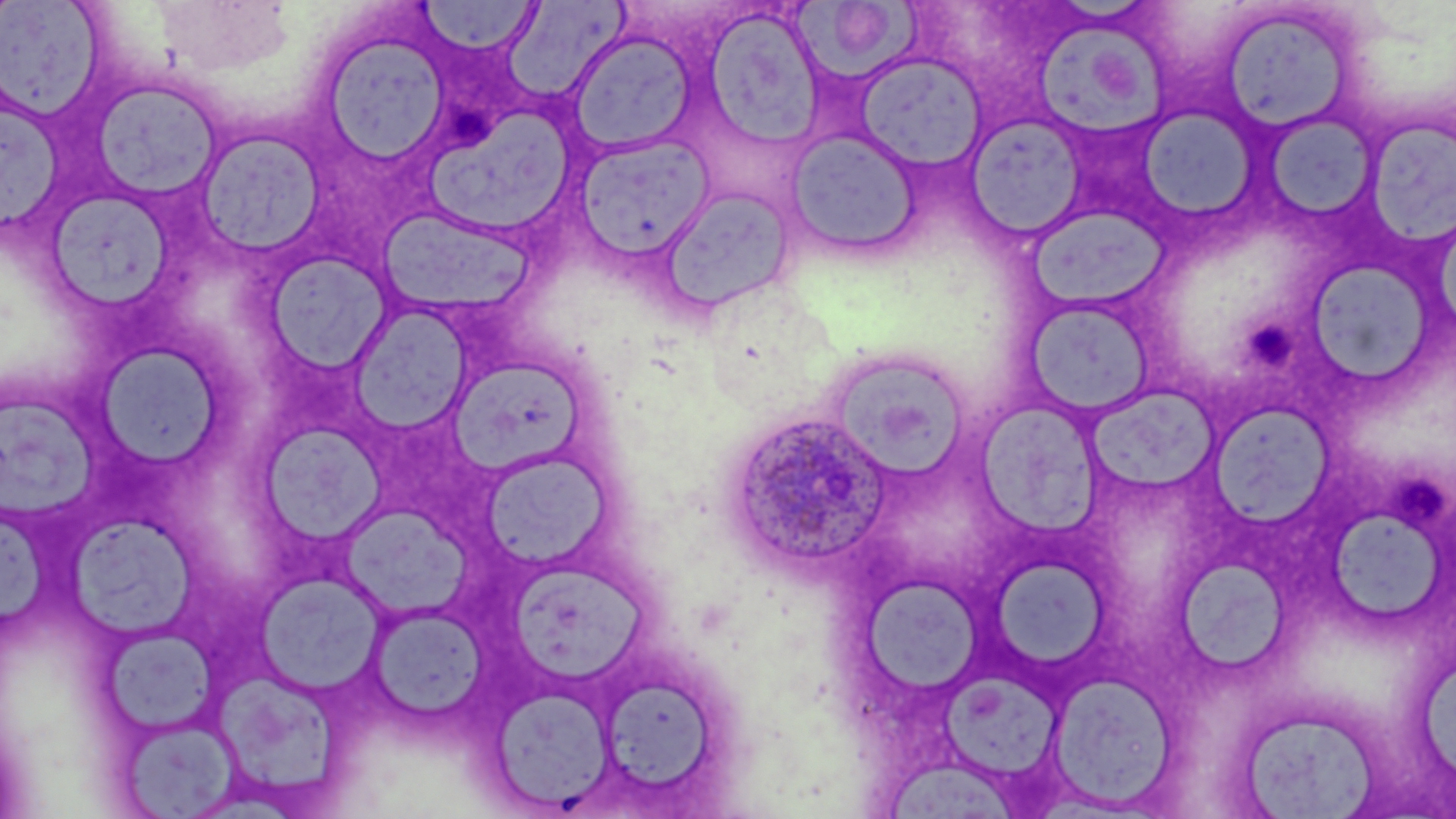 Approximate bounding boxes as (x1,y1)-(x2,y2) corner pairs in pixels. Plasmodium ovale-infected red blood cell locations: (721,409)-(895,576). Platelet locations: (445,109)-(500,153), (1247,317)-(1294,369), (1392,479)-(1451,529). Uninfected red blood cell locations: (416,0)-(542,57), (1,1)-(107,122), (503,2)-(629,107), (788,2)-(930,81), (1213,4)-(1362,136), (704,8)-(825,150), (1038,21)-(1172,139), (314,28)-(450,168), (568,32)-(697,154), (855,52)-(987,172), (85,79)-(223,204), (4,104)-(68,233), (421,104)-(578,230), (1135,107)-(1258,222), (1262,111)-(1379,226), (964,115)-(1085,240), (1365,116)-(1456,243), (785,127)-(922,259), (193,129)-(326,259), (573,133)-(715,261), (656,187)-(797,315), (55,192)-(172,306), (1029,206)-(1166,309), (379,210)-(536,312), (264,252)-(393,374), (1304,259)-(1438,389), (1023,297)-(1156,417), (346,301)-(476,436), (90,341)-(226,472), (824,348)-(970,480), (448,357)-(589,477), (1084,383)-(1220,500), (4,395)-(99,523), (977,399)-(1106,541), (1213,401)-(1337,529), (263,423)-(385,548), (484,450)-(610,574), (343,501)-(471,620), (4,514)-(54,635), (70,517)-(206,643), (1329,518)-(1448,621), (993,554)-(1105,670), (1181,557)-(1291,668), (508,558)-(650,690), (255,576)-(391,692), (865,578)-(980,688), (366,603)-(489,723), (102,624)-(220,737), (1421,666)-(1456,772), (938,670)-(1056,774), (1049,671)-(1180,809), (214,675)-(353,797), (601,678)-(721,793), (491,685)-(614,810), (1234,705)-(1384,817), (117,716)-(241,817), (889,763)-(1019,819). Slide-level diagnosis: Plasmodium ovale. May-Grünwald-Giemsa-stained preparation. Single field of view. Light microscopy. 1000x magnification. Thin blood film. Image is 1456×819 pixels.